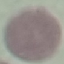

Summary:
  - Result: no malaria parasites detected
  - Stain: Giemsa
  - Preparation: thin blood film
  - Image type: automatically extracted cell patch, resized to 64 × 64 pixels
  - Capture: smartphone through the microscope eyepiece